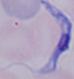
Summary:
  - Identification: trypanosome
  - Magnification: 1000x
  - Modality: micrograph